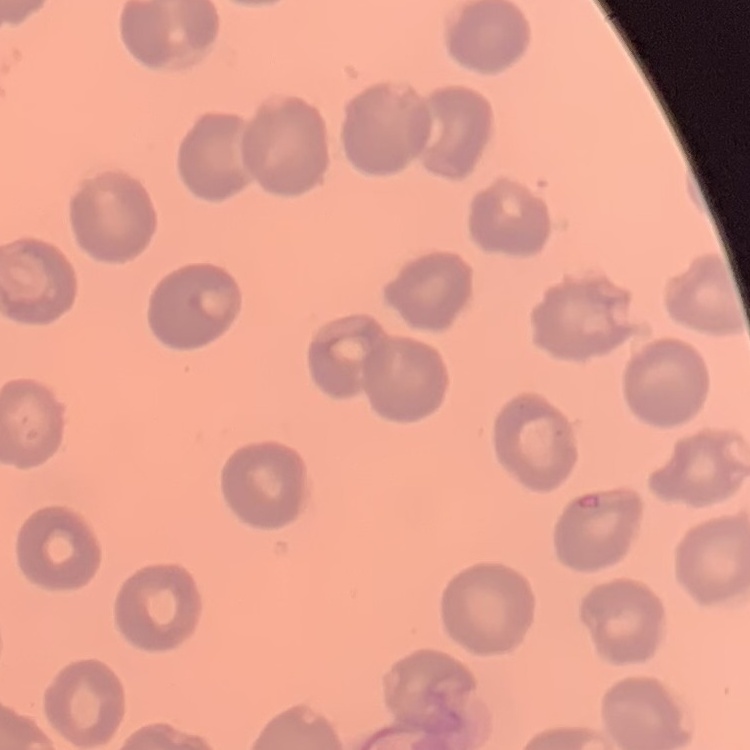
Summary:
  - Erythrocyte morphology: no rouleaux formation
  - Image type: one tile cut from a larger photomicrograph
  - Preparation: thin blood film
  - Stain: Field's or Giemsa